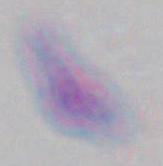

Toxoplasma gondii is seen. Micrograph. Captured at 1000x magnification.